Report the malaria status of this cell.
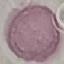
Uninfected.

Summary:
  - Preparation: thin blood film
  - Image type: automatically extracted cell patch, resized to 64 × 64 pixels
  - Stain: Giemsa
  - Capture: smartphone camera at the microscope eyepiece